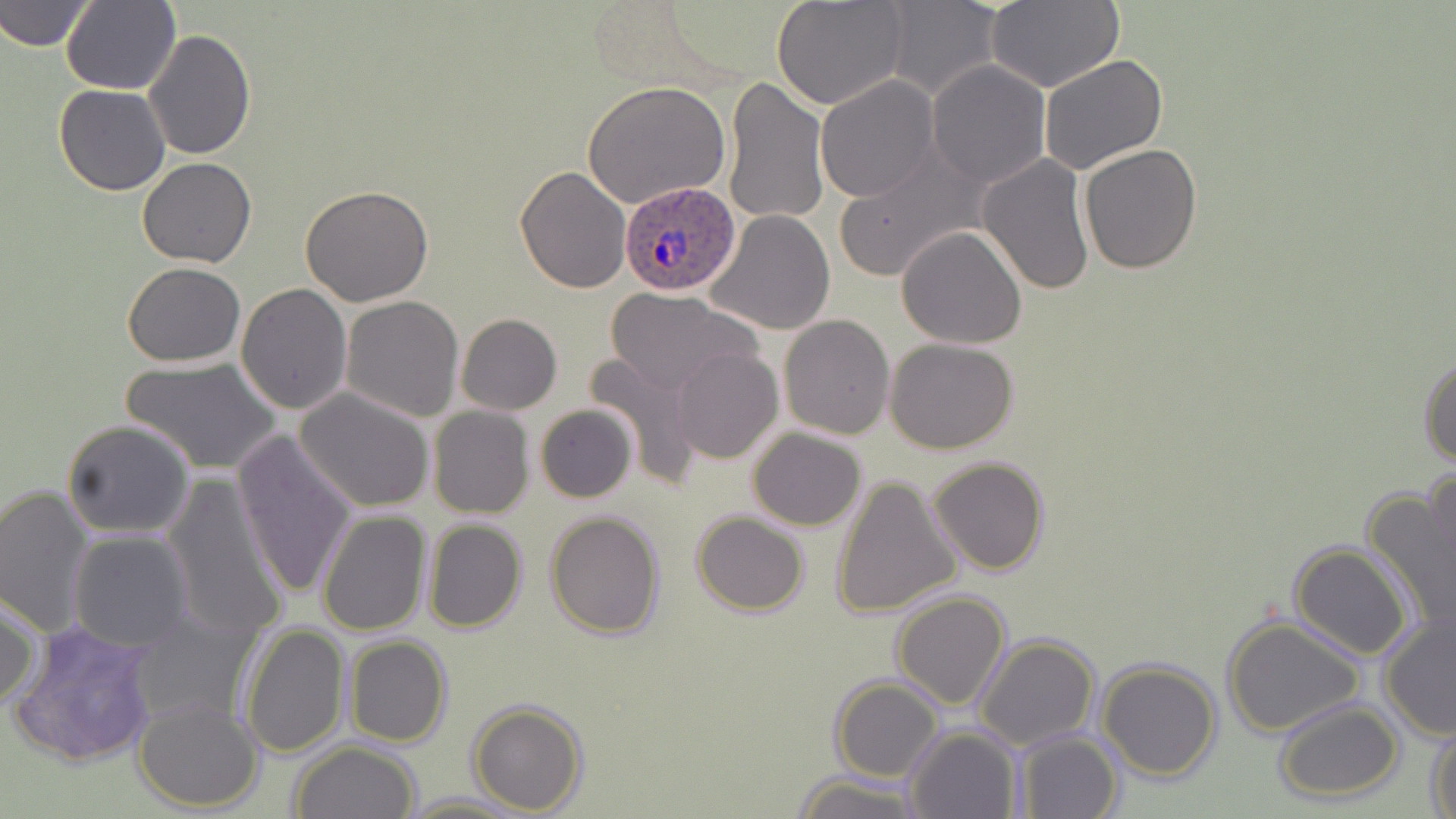
Approximate bounding boxes as named x1/y1/x2/y2 corners in pixels. Uninfected red blood cell locations: (x1=772, y1=0, x2=912, y2=110), (x1=1, y1=1, x2=96, y2=51), (x1=60, y1=1, x2=180, y2=95), (x1=879, y1=1, x2=1003, y2=101), (x1=982, y1=3, x2=1122, y2=91), (x1=143, y1=28, x2=257, y2=161), (x1=1039, y1=51, x2=1169, y2=175), (x1=927, y1=61, x2=1049, y2=187), (x1=721, y1=75, x2=828, y2=227), (x1=814, y1=76, x2=941, y2=203), (x1=584, y1=82, x2=731, y2=212), (x1=55, y1=84, x2=170, y2=196), (x1=1078, y1=143, x2=1204, y2=274), (x1=833, y1=146, x2=985, y2=284), (x1=976, y1=153, x2=1095, y2=297), (x1=137, y1=157, x2=255, y2=269), (x1=515, y1=166, x2=632, y2=294), (x1=300, y1=184, x2=434, y2=306), (x1=705, y1=210, x2=837, y2=334), (x1=897, y1=226, x2=1026, y2=350), (x1=121, y1=262, x2=247, y2=366), (x1=237, y1=282, x2=352, y2=415), (x1=606, y1=288, x2=760, y2=396), (x1=341, y1=295, x2=465, y2=421), (x1=456, y1=313, x2=561, y2=415), (x1=779, y1=314, x2=895, y2=439), (x1=885, y1=338, x2=1019, y2=455), (x1=671, y1=348, x2=783, y2=465), (x1=583, y1=353, x2=704, y2=482), (x1=1418, y1=354, x2=1456, y2=470), (x1=123, y1=357, x2=280, y2=474), (x1=294, y1=388, x2=437, y2=514), (x1=535, y1=403, x2=637, y2=503), (x1=427, y1=406, x2=534, y2=518), (x1=62, y1=419, x2=195, y2=537), (x1=748, y1=428, x2=866, y2=530), (x1=232, y1=432, x2=360, y2=600), (x1=928, y1=456, x2=1051, y2=575), (x1=1423, y1=463, x2=1456, y2=596), (x1=163, y1=474, x2=288, y2=643), (x1=831, y1=475, x2=962, y2=619), (x1=0, y1=485, x2=97, y2=636), (x1=1364, y1=487, x2=1456, y2=637), (x1=316, y1=509, x2=431, y2=635), (x1=545, y1=510, x2=665, y2=640), (x1=691, y1=511, x2=810, y2=615), (x1=423, y1=518, x2=528, y2=633), (x1=68, y1=531, x2=194, y2=651), (x1=1287, y1=542, x2=1415, y2=660), (x1=891, y1=591, x2=1010, y2=710), (x1=0, y1=592, x2=41, y2=714), (x1=128, y1=606, x2=260, y2=732), (x1=1377, y1=608, x2=1456, y2=742), (x1=1222, y1=616, x2=1367, y2=738), (x1=9, y1=618, x2=161, y2=768), (x1=241, y1=623, x2=350, y2=760), (x1=974, y1=635, x2=1100, y2=751), (x1=344, y1=636, x2=452, y2=748), (x1=1097, y1=659, x2=1221, y2=781), (x1=828, y1=679, x2=944, y2=782), (x1=1273, y1=698, x2=1402, y2=803), (x1=134, y1=699, x2=265, y2=813), (x1=467, y1=701, x2=588, y2=814), (x1=1428, y1=721, x2=1456, y2=819), (x1=904, y1=725, x2=1022, y2=818), (x1=1012, y1=732, x2=1123, y2=819), (x1=290, y1=741, x2=423, y2=819), (x1=792, y1=771, x2=920, y2=819), (x1=403, y1=792, x2=527, y2=818). Plasmodium ovale-infected red blood cell locations: (x1=619, y1=182, x2=742, y2=297). Slide-level diagnosis: Plasmodium ovale. Light microscopy. 1000x magnification. Thin blood smear. Image is 1456×819 pixels. May-Grünwald-Giemsa stain. Single field of view.